Comment on the morphology of the red blood cells.
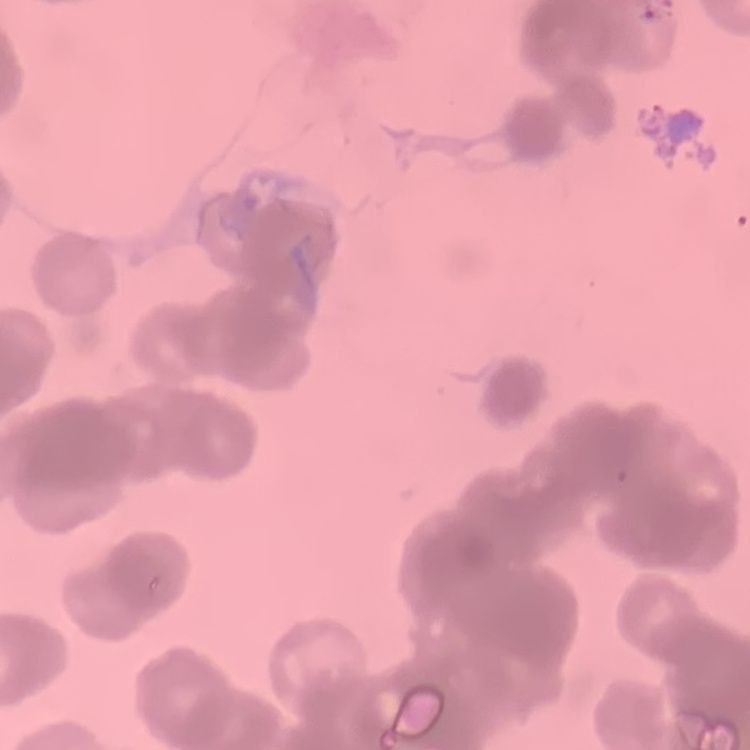

Rouleaux formation.

Square crop of a larger photomicrograph. Field's or Giemsa stain. Thin blood smear.